Outline each blood parasite and name the species.
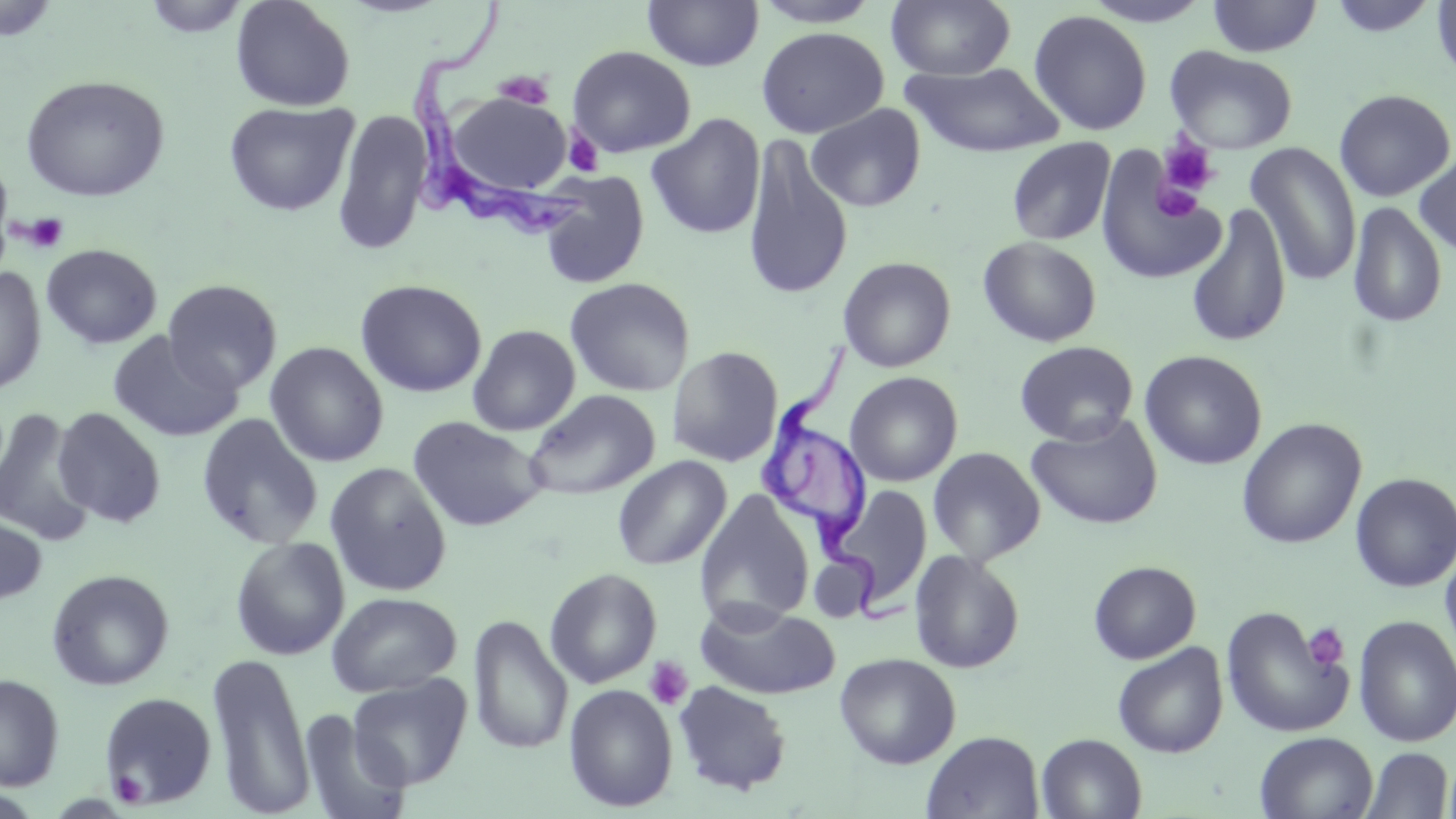
Approximate bounding boxes as (x1, y1, x2, y2) in pixels.
Trypanosoma brucei: (407, 0, 589, 243), (755, 331, 909, 624).
No Plasmodium falciparum, Plasmodium ovale, Plasmodium malariae, Plasmodium vivax, or Babesia divergens observed.

Summary:
  - Platelet locations: (493, 70, 555, 110), (563, 128, 603, 176), (1158, 138, 1219, 197), (1155, 182, 1200, 220), (20, 212, 69, 254), (1303, 622, 1349, 671), (644, 656, 693, 711), (110, 770, 149, 806)
  - Uninfected red blood cell locations: (141, 0, 252, 38), (230, 0, 356, 112), (642, 0, 764, 71), (749, 0, 885, 28), (886, 0, 1016, 81), (1081, 0, 1216, 27), (1206, 0, 1323, 57), (1325, 0, 1442, 38), (1431, 0, 1456, 85), (1, 1, 61, 41), (1029, 10, 1152, 136), (756, 27, 889, 138), (1164, 44, 1298, 153), (568, 45, 696, 158), (903, 62, 1066, 158), (20, 75, 170, 203), (1334, 88, 1456, 202), (448, 93, 571, 195), (223, 101, 359, 216), (806, 103, 926, 213), (332, 109, 432, 256), (646, 113, 766, 240), (741, 134, 854, 302), (1006, 138, 1116, 246), (1244, 142, 1361, 288), (1414, 149, 1456, 259), (1094, 150, 1226, 286), (536, 173, 649, 289), (1347, 201, 1448, 329), (1185, 202, 1292, 349), (978, 237, 1101, 347), (41, 244, 162, 349), (838, 256, 956, 373), (0, 265, 46, 396), (564, 277, 695, 397), (162, 279, 282, 394), (355, 279, 486, 398), (468, 325, 581, 436), (107, 331, 242, 443), (1014, 341, 1139, 445), (265, 342, 389, 467), (667, 346, 783, 467), (1140, 350, 1266, 470), (845, 371, 963, 486), (524, 389, 660, 501), (52, 406, 166, 527), (0, 409, 95, 545), (196, 413, 323, 549), (1025, 413, 1163, 530), (407, 417, 548, 531), (1237, 417, 1366, 549), (927, 446, 1046, 566), (612, 455, 732, 571), (324, 462, 452, 597), (1350, 472, 1456, 592), (824, 485, 932, 608), (695, 491, 815, 629), (0, 509, 47, 606), (230, 537, 349, 660), (1440, 540, 1456, 669), (909, 550, 1025, 673), (810, 554, 875, 622), (1088, 561, 1200, 664), (545, 567, 662, 689), (46, 569, 174, 691), (326, 591, 461, 698), (693, 599, 840, 700), (1221, 606, 1353, 739), (467, 614, 573, 755), (1352, 615, 1455, 747), (1112, 642, 1228, 758), (208, 651, 315, 818), (835, 652, 961, 769), (347, 673, 472, 790), (0, 674, 64, 791), (673, 680, 792, 796), (563, 683, 678, 812), (99, 692, 217, 809), (299, 708, 412, 819), (922, 731, 1044, 819), (1254, 732, 1378, 819), (1036, 733, 1147, 819), (1359, 746, 1454, 819)
  - Slide-level diagnosis: Trypanosoma brucei
  - Field of view: one of a larger specimen
  - Preparation: thin blood smear
  - Modality: optical microscopy
  - Image size: 1456×819 pixels
  - Magnification: 1000x
  - Stain: May-Grünwald-Giemsa